Report the malaria status of this cell.
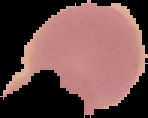

It is uninfected.

Summary:
  - Image size: 148×118 pixels
  - Preparation: thin blood smear
  - Image type: segmented cell region with the area outside set to black